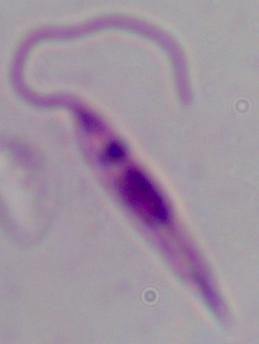

Summary:
  - Identification: Leishmania
  - Magnification: 1000x
  - Modality: micrograph